Locate every Plasmodium parasite.
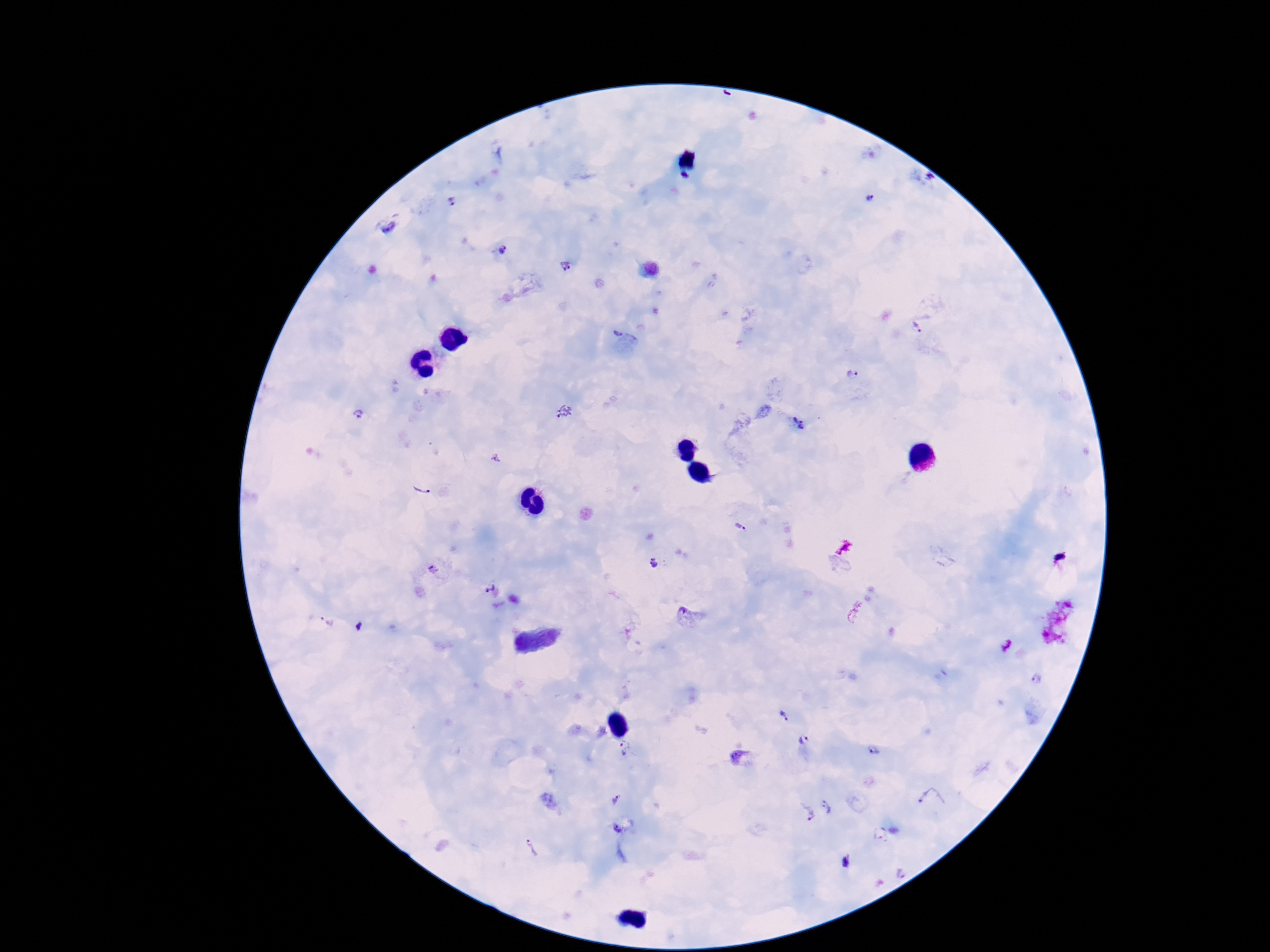
Approximate object centers, in pixels from the top-left corner.
Plasmodium parasites: (x=869, y=198), (x=451, y=201), (x=505, y=250), (x=565, y=267), (x=917, y=326), (x=614, y=334), (x=852, y=374), (x=565, y=412), (x=361, y=413), (x=798, y=422), (x=495, y=458), (x=422, y=492), (x=741, y=528), (x=653, y=563), (x=434, y=571), (x=486, y=586), (x=685, y=615), (x=1038, y=678), (x=784, y=715), (x=803, y=739), (x=626, y=748), (x=872, y=749), (x=929, y=797), (x=615, y=798), (x=830, y=807), (x=807, y=813), (x=617, y=827), (x=534, y=850).

field_of_view: one from this slide
magnification: 100x
patient_malaria_status: infected
preparation: thick blood smear
image_size: 1270×952 pixels
stain: Giemsa
capture: smartphone camera through the microscope eyepiece